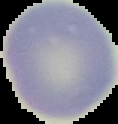
Segmented cell region on a black background. Result: negative for malaria parasites. Image is 118×124 pixels. From a thin blood film.